Point out every malaria parasite and every leukocyte.
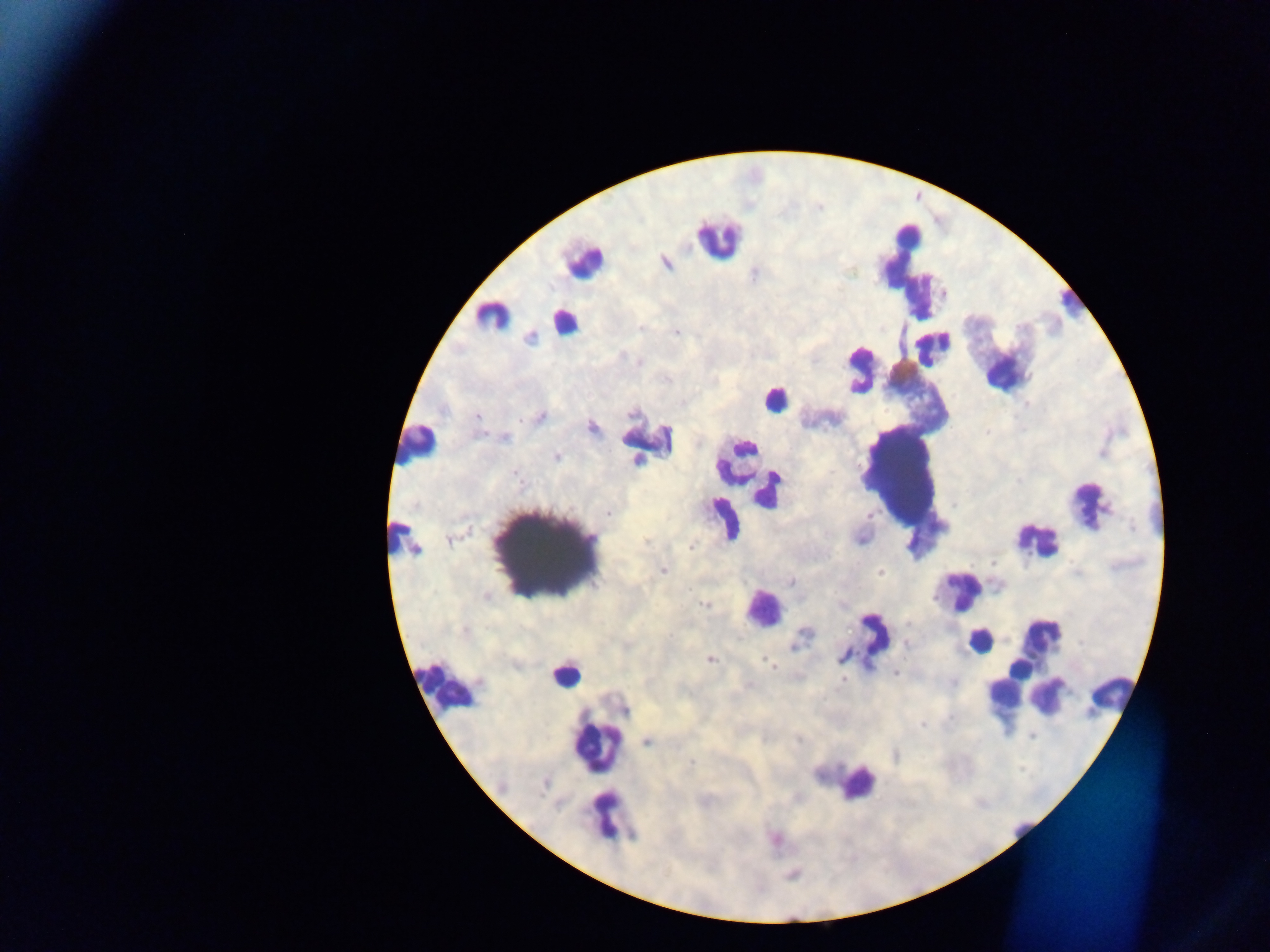
Approximate centers as [x, y] in pixels.
Malaria parasites: [665, 262], [943, 293], [677, 332], [530, 337], [638, 362], [540, 416], [477, 417], [591, 427], [504, 437], [556, 457], [608, 512], [691, 547], [663, 570], [880, 572], [789, 581], [840, 603], [705, 604], [905, 644], [710, 659], [770, 665], [895, 673], [843, 679], [749, 686], [922, 724], [1031, 735], [647, 741], [775, 839].
Leukocytes: [908, 236], [717, 239], [583, 260], [1071, 301], [493, 316], [564, 322], [934, 347], [861, 367], [903, 371], [1007, 372], [773, 400], [649, 442], [417, 443], [743, 449], [738, 457], [768, 491], [1089, 505], [723, 520], [404, 538], [1037, 539], [960, 591], [763, 608], [1040, 637], [871, 638], [979, 640], [1019, 670], [566, 674], [446, 688], [1006, 690], [1110, 692], [1048, 695], [597, 749], [858, 783], [610, 817], [1022, 829].

image_size: 1270×952 pixels
preparation: thick blood smear
capture: mobile-phone photograph through a microscope
field_of_view: single
country: Ghana